Comment on the morphology of the red blood cells.
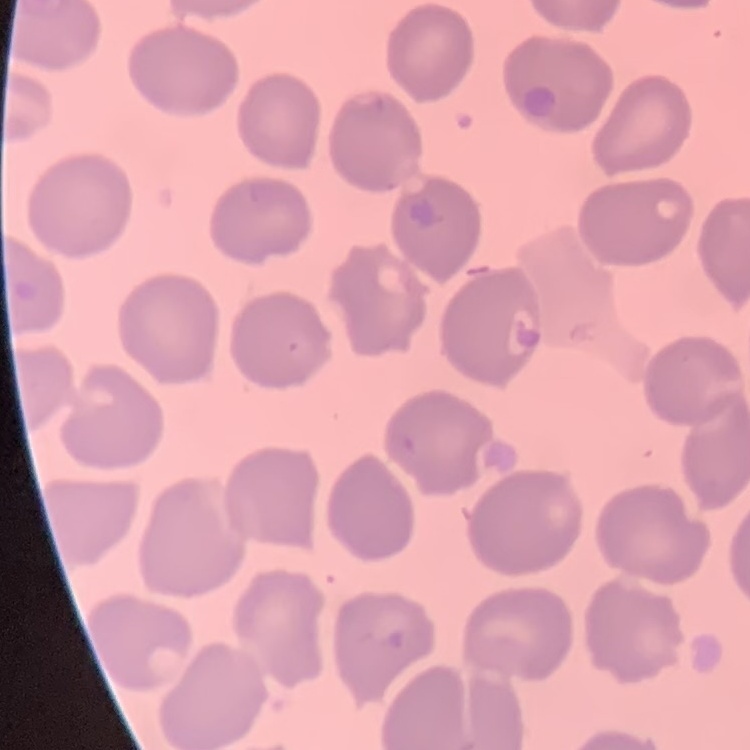
No rouleaux formation.

{
  "stain": "Field's or Giemsa",
  "preparation": "thin blood film",
  "image_type": "one tile cut from a larger photomicrograph"
}